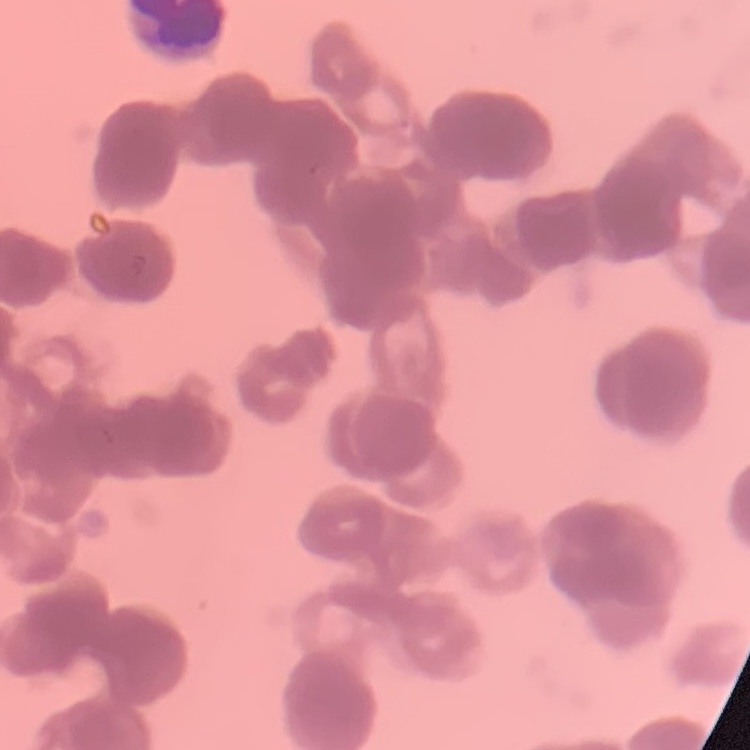
erythrocyte morphology = rouleaux formation
image type = square crop of a larger photomicrograph
preparation = thin peripheral smear
stain = Field's or Giemsa